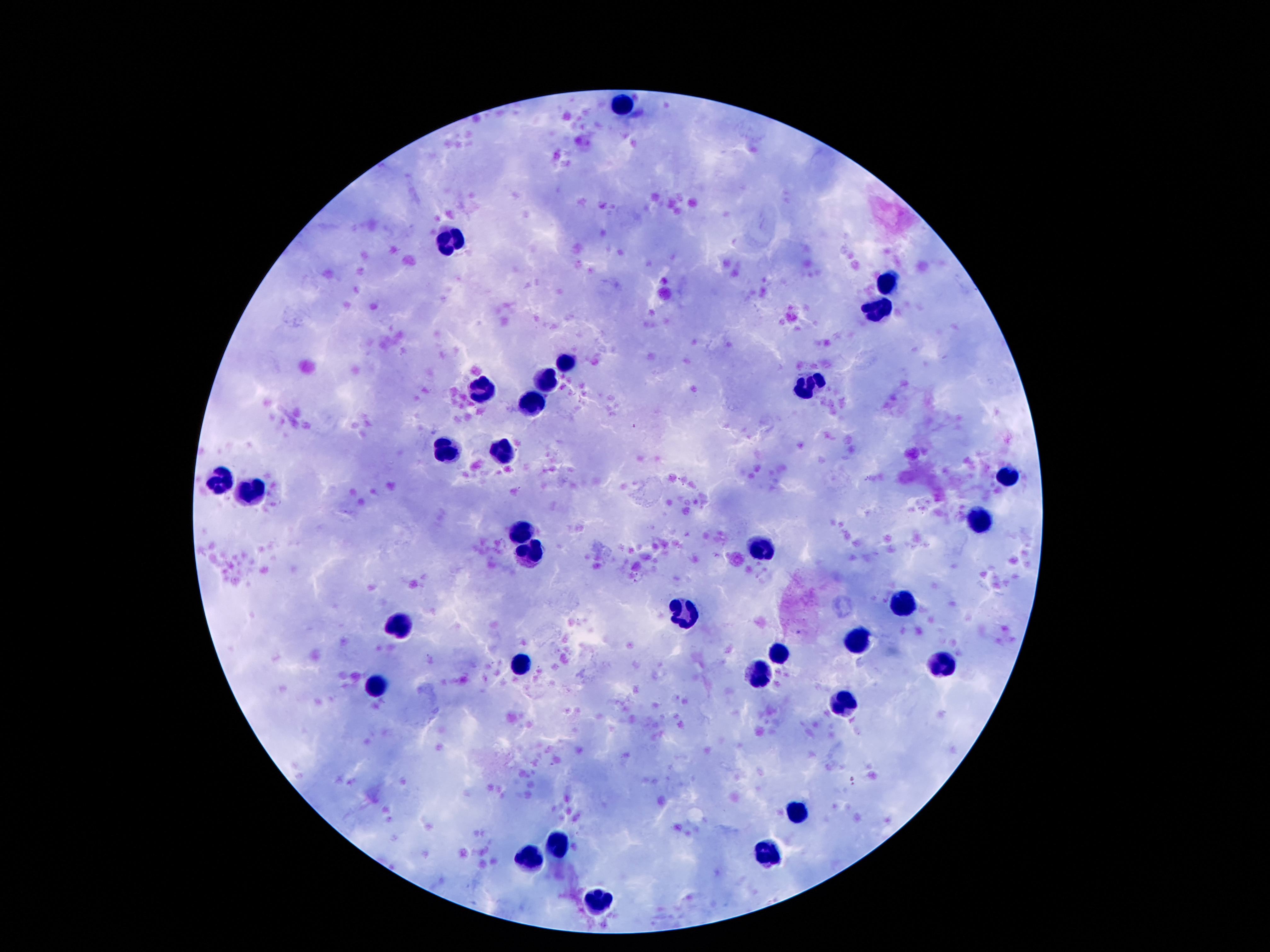
Approximate centers as (x, y) in pixels. Leukocyte locations: (625, 102), (455, 238), (886, 284), (879, 310), (566, 360), (549, 378), (480, 389), (806, 389), (531, 404), (503, 452), (445, 453), (1007, 476), (218, 482), (253, 494), (980, 522), (522, 530), (764, 549), (529, 554), (906, 605), (684, 613), (400, 624), (858, 642), (780, 653), (524, 667), (938, 667), (759, 672), (375, 688), (844, 699), (797, 810), (558, 846), (772, 852), (529, 859), (598, 901). 100x magnification. Single field of view. Thick blood film. Patient malaria status: not infected. Photographed through the microscope eyepiece with a smartphone camera. Image is 1270×952 pixels. Giemsa-stained preparation.